Report the malaria status of this cell.
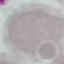

It is uninfected.

Summary:
  - Preparation: thin smear
  - Image type: cell patch, automatically extracted from a larger field of view and resized to 64 × 64 pixels
  - Capture: smartphone through the microscope eyepiece
  - Stain: Giemsa